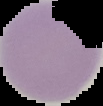
Summary:
  - Image type: segmented cell region on a black background
  - Image size: 103×106 pixels
  - Malaria status: uninfected
  - Preparation: thin blood film